Give the extent of all Plasmodium ovale-infected red blood cells.
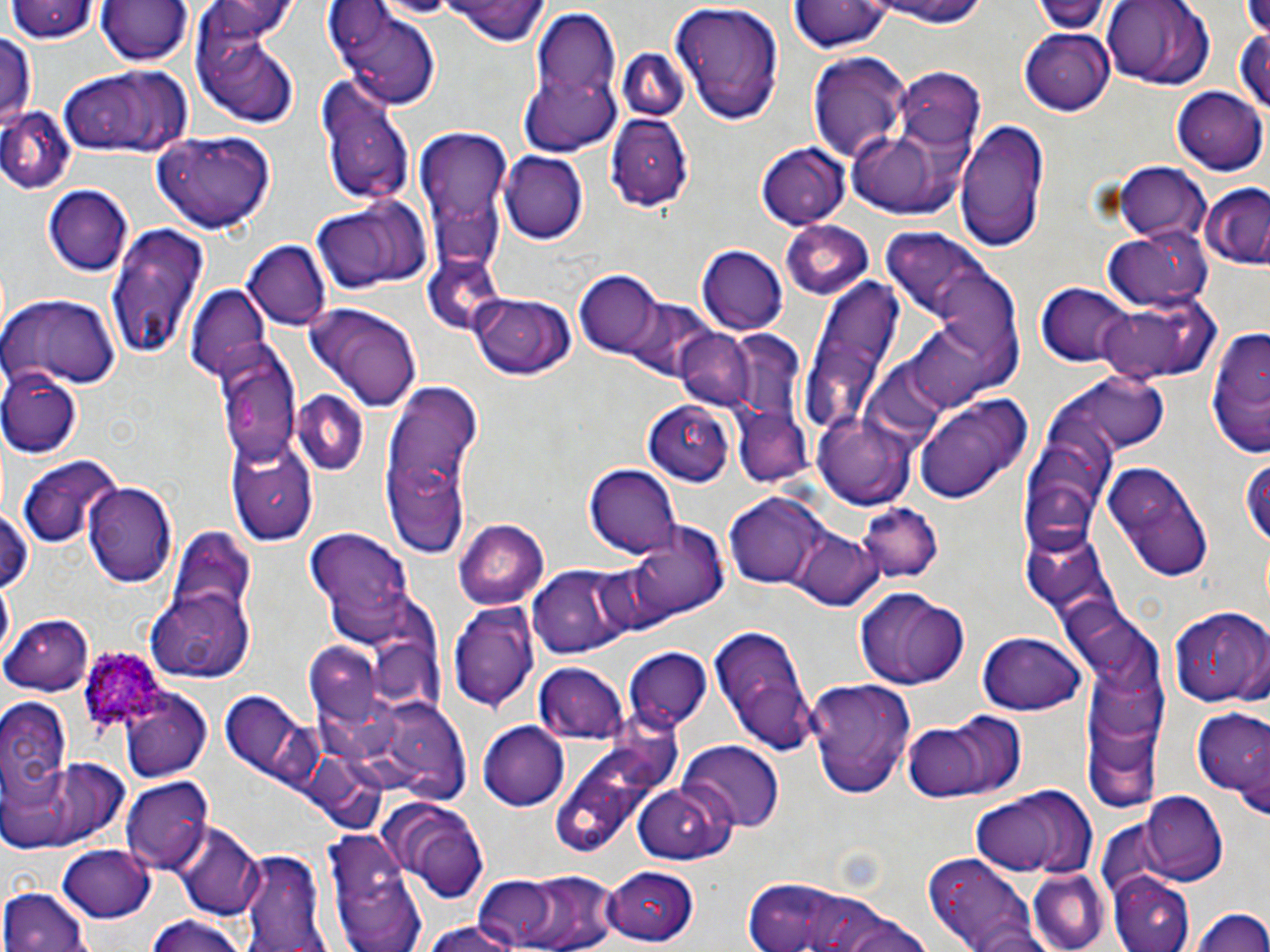
Approximate bounding boxes as [x1, y1, x2, y2] in pixels.
Plasmodium ovale-infected red blood cells: [73, 647, 180, 744].

Uninfected red blood cell locations: [7, 0, 98, 44], [92, 0, 195, 67], [443, 0, 548, 45], [860, 0, 997, 27], [1032, 0, 1111, 33], [1098, 0, 1215, 90], [792, 1, 890, 55], [194, 2, 300, 49], [671, 2, 787, 126], [333, 6, 439, 111], [521, 10, 626, 153], [193, 15, 302, 127], [1233, 23, 1269, 126], [1022, 29, 1116, 113], [0, 33, 37, 133], [806, 49, 911, 164], [622, 50, 688, 122], [898, 65, 984, 148], [59, 67, 196, 159], [316, 77, 415, 206], [1173, 86, 1268, 172], [0, 108, 75, 195], [606, 114, 694, 210], [955, 116, 1050, 247], [843, 123, 971, 219], [155, 129, 275, 232], [417, 133, 513, 231], [756, 140, 849, 228], [500, 152, 590, 243], [1116, 163, 1212, 247], [44, 183, 136, 277], [1200, 186, 1270, 271], [311, 197, 430, 294], [426, 201, 510, 282], [781, 221, 874, 300], [104, 224, 211, 362], [1103, 227, 1210, 310], [244, 239, 331, 332], [696, 246, 786, 334], [423, 260, 510, 331], [928, 264, 1027, 366], [573, 273, 659, 355], [796, 280, 905, 447], [185, 281, 272, 380], [1038, 283, 1133, 365], [0, 293, 120, 391], [474, 293, 575, 379], [614, 294, 719, 384], [1092, 296, 1212, 384], [304, 300, 424, 415], [1201, 319, 1270, 459], [677, 330, 755, 411], [218, 347, 304, 469], [2, 368, 83, 457], [1090, 369, 1171, 448], [381, 380, 487, 553], [292, 392, 367, 478], [915, 392, 1033, 503], [642, 400, 734, 486], [734, 410, 809, 490], [1047, 410, 1119, 506], [816, 411, 914, 506], [228, 441, 318, 544], [1242, 450, 1270, 550], [18, 453, 120, 550], [1100, 460, 1215, 583], [586, 463, 682, 559], [85, 480, 177, 590], [1026, 486, 1105, 555], [726, 493, 825, 590], [857, 504, 941, 583], [0, 505, 30, 593], [454, 518, 550, 608], [307, 528, 414, 640], [791, 529, 882, 610], [626, 530, 727, 627], [162, 531, 258, 639], [1024, 542, 1111, 604], [528, 565, 630, 659], [853, 588, 970, 690], [149, 590, 254, 681], [451, 604, 539, 712], [1171, 604, 1270, 705], [6, 614, 94, 696], [707, 625, 818, 754], [981, 631, 1085, 713], [302, 644, 389, 722], [625, 647, 715, 733], [535, 665, 627, 745], [1092, 671, 1168, 740], [813, 679, 920, 795], [220, 689, 315, 786], [120, 690, 211, 781], [366, 695, 471, 804], [0, 698, 71, 811], [1193, 702, 1269, 809], [913, 710, 1030, 800], [1089, 719, 1164, 815], [479, 721, 571, 810], [546, 722, 679, 857], [678, 740, 785, 833], [10, 756, 131, 849], [122, 776, 212, 872], [633, 782, 736, 864], [968, 787, 1096, 878], [1139, 792, 1229, 885], [380, 797, 492, 901], [1095, 816, 1187, 902], [173, 820, 264, 921], [324, 831, 424, 952], [59, 844, 154, 920], [239, 847, 328, 952], [923, 849, 1047, 952], [603, 865, 700, 945], [483, 867, 620, 951], [1026, 870, 1110, 952], [1110, 873, 1194, 951], [738, 875, 864, 952], [1, 886, 94, 952], [1190, 905, 1269, 952], [831, 911, 935, 952], [143, 915, 251, 952], [420, 923, 526, 952]. Slide-level diagnosis: Plasmodium ovale. May-Grünwald-Giemsa-stained preparation. 1000x magnification. Image is 1270×952 pixels. One field of a larger specimen. Light microscopy. Thin blood smear.